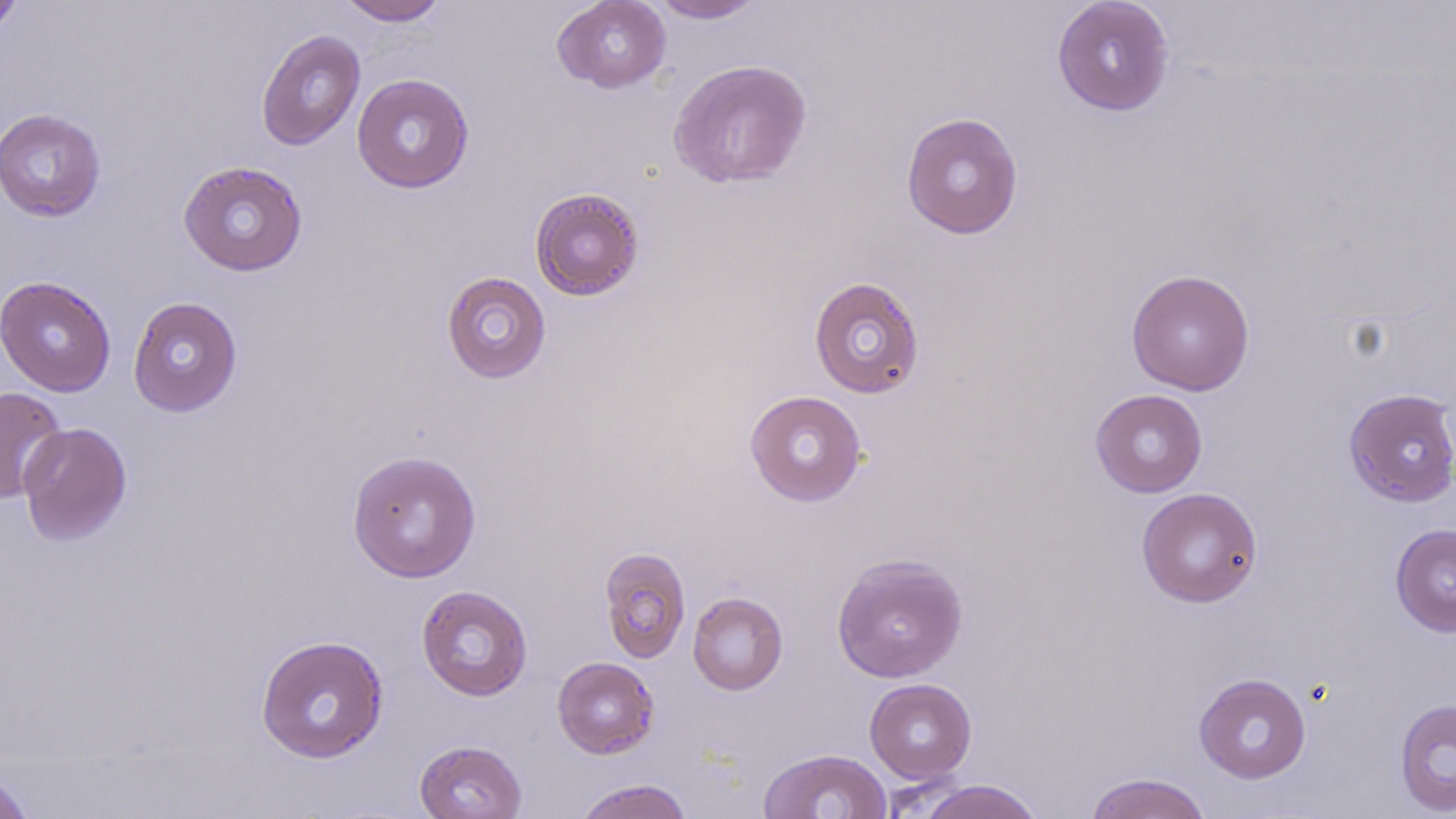

{
  "slide_level_diagnosis": "no evidence of blood parasites",
  "modality": "optical microscopy",
  "preparation": "thin blood smear",
  "field_of_view": "single",
  "image_size": "1456×819 pixels",
  "stain": "May-Grünwald-Giemsa",
  "magnification": "1000x",
  "uninfected_red_blood_cell_locations": "approximate bounding boxes as named x1/y1/x2/y2 corners in pixels: (x1=336, y1=0, x2=450, y2=26), (x1=552, y1=0, x2=671, y2=93), (x1=649, y1=0, x2=767, y2=23), (x1=1051, y1=0, x2=1175, y2=116), (x1=0, y1=1, x2=23, y2=38), (x1=256, y1=28, x2=366, y2=151), (x1=667, y1=59, x2=813, y2=189), (x1=352, y1=73, x2=474, y2=193), (x1=0, y1=107, x2=106, y2=222), (x1=901, y1=111, x2=1024, y2=240), (x1=178, y1=160, x2=308, y2=277), (x1=529, y1=187, x2=645, y2=301), (x1=1126, y1=268, x2=1255, y2=396), (x1=441, y1=271, x2=551, y2=384), (x1=808, y1=275, x2=925, y2=399), (x1=0, y1=276, x2=116, y2=397), (x1=127, y1=296, x2=243, y2=417), (x1=0, y1=387, x2=67, y2=503), (x1=1090, y1=388, x2=1208, y2=497), (x1=1343, y1=388, x2=1456, y2=508), (x1=744, y1=390, x2=867, y2=507), (x1=17, y1=422, x2=132, y2=547), (x1=346, y1=449, x2=482, y2=583), (x1=1136, y1=487, x2=1263, y2=608), (x1=1390, y1=523, x2=1456, y2=637), (x1=598, y1=546, x2=691, y2=664), (x1=830, y1=552, x2=968, y2=683), (x1=417, y1=585, x2=533, y2=701), (x1=687, y1=591, x2=788, y2=695), (x1=255, y1=634, x2=389, y2=763), (x1=552, y1=656, x2=659, y2=759), (x1=1193, y1=673, x2=1311, y2=783), (x1=864, y1=678, x2=977, y2=783), (x1=1394, y1=698, x2=1456, y2=815), (x1=414, y1=739, x2=527, y2=819), (x1=757, y1=749, x2=892, y2=819), (x1=0, y1=766, x2=37, y2=819), (x1=1083, y1=772, x2=1213, y2=819), (x1=574, y1=778, x2=694, y2=819), (x1=917, y1=779, x2=1045, y2=819)"
}